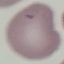

{
  "malaria_status": "uninfected",
  "stain": "Giemsa",
  "image_type": "cell patch, automatically extracted from a larger field of view and resized to 64 × 64 pixels",
  "capture": "smartphone through the microscope eyepiece",
  "preparation": "thin blood smear"
}